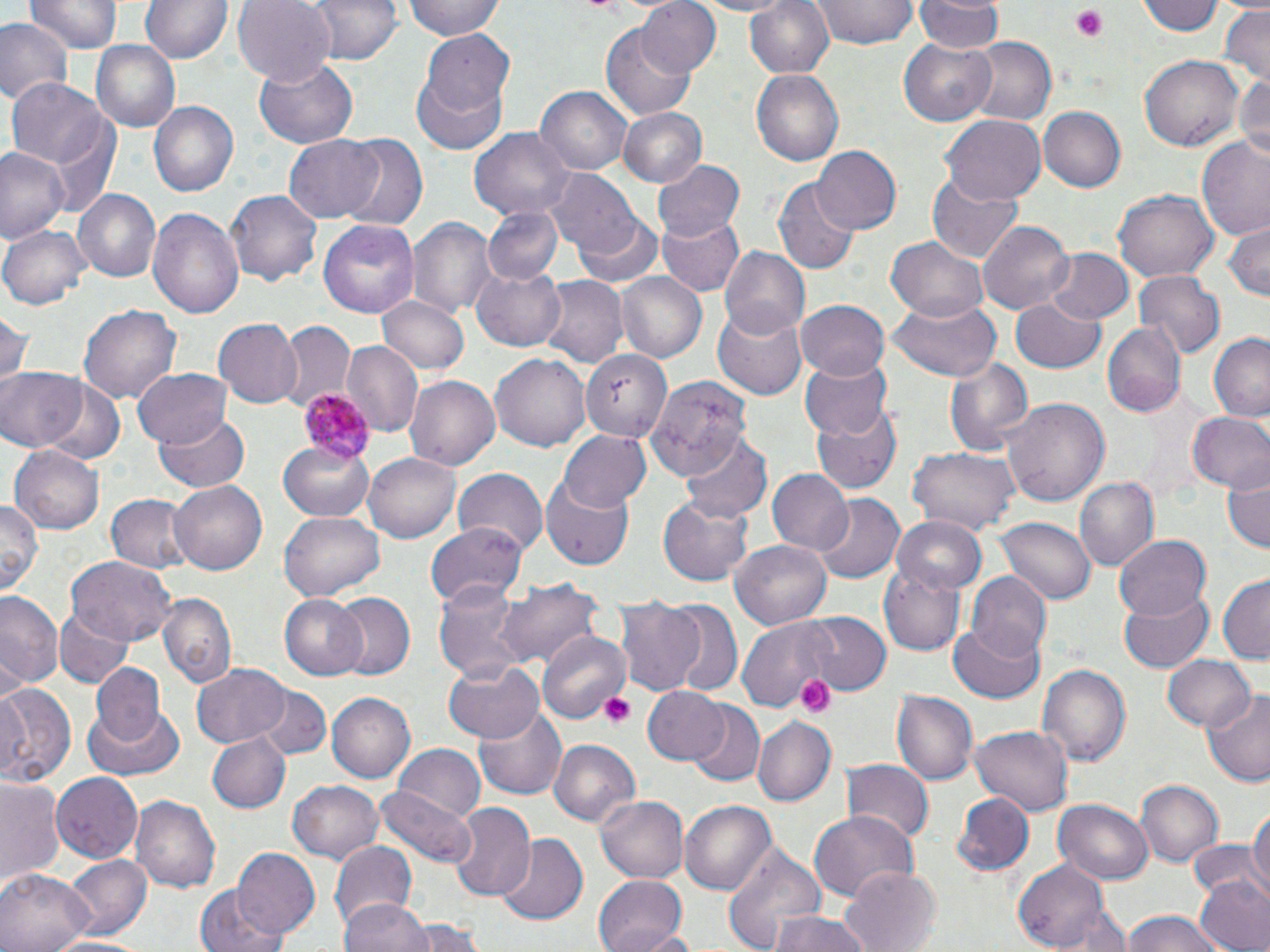 Approximate bounding boxes as (x1, y1, x2, y2) in pixels. Uninfected red blood cell locations: (27, 0, 120, 54), (139, 0, 233, 64), (232, 0, 335, 85), (305, 0, 404, 64), (402, 0, 507, 41), (636, 0, 721, 79), (684, 0, 803, 17), (742, 0, 835, 80), (812, 0, 917, 50), (1138, 0, 1225, 38), (915, 1, 1003, 55), (415, 3, 505, 82), (1217, 4, 1270, 86), (0, 18, 72, 103), (602, 22, 696, 121), (418, 29, 514, 118), (965, 38, 1056, 125), (898, 40, 994, 125), (91, 42, 179, 134), (1141, 54, 1244, 152), (254, 58, 359, 149), (414, 65, 509, 155), (750, 69, 844, 166), (7, 76, 112, 177), (1232, 77, 1269, 162), (536, 85, 634, 177), (149, 100, 240, 197), (1040, 105, 1127, 193), (616, 108, 706, 187), (942, 114, 1046, 205), (470, 129, 574, 221), (283, 132, 386, 223), (336, 133, 430, 228), (1196, 137, 1270, 243), (813, 145, 902, 234), (0, 146, 67, 244), (653, 160, 748, 243), (925, 170, 1025, 265), (549, 172, 643, 259), (775, 177, 860, 274), (73, 189, 162, 284), (225, 190, 324, 285), (1112, 191, 1219, 284), (149, 205, 245, 323), (483, 208, 562, 285), (573, 209, 665, 290), (657, 216, 747, 296), (409, 217, 495, 317), (1224, 218, 1269, 301), (319, 220, 420, 318), (979, 220, 1073, 316), (1, 225, 91, 309), (888, 236, 990, 321), (720, 247, 811, 340), (1043, 248, 1132, 328), (474, 264, 568, 351), (613, 269, 707, 362), (1134, 271, 1225, 360), (538, 274, 628, 369), (377, 295, 469, 376), (886, 296, 1002, 383), (796, 298, 893, 381), (1011, 299, 1107, 375), (80, 304, 182, 405), (713, 304, 810, 397), (0, 308, 30, 390), (215, 318, 304, 408), (276, 320, 355, 409), (1103, 320, 1185, 419), (1208, 332, 1270, 421), (577, 338, 669, 443), (344, 341, 422, 438), (491, 353, 590, 452), (801, 355, 893, 437), (945, 356, 1032, 457), (133, 366, 230, 449), (0, 367, 84, 452), (405, 374, 500, 472), (647, 379, 749, 480), (40, 381, 125, 467), (1003, 396, 1109, 509), (812, 403, 903, 494), (153, 411, 247, 492), (1185, 412, 1270, 494), (556, 428, 652, 512), (681, 433, 771, 522), (277, 441, 376, 521), (10, 444, 105, 533), (909, 448, 1019, 533), (365, 450, 465, 544), (455, 469, 546, 552), (769, 469, 854, 553), (1222, 469, 1268, 554), (1074, 476, 1159, 570), (540, 477, 634, 569), (169, 479, 269, 574), (812, 492, 904, 585), (105, 493, 191, 570), (658, 497, 754, 586), (0, 499, 41, 593), (281, 513, 384, 600), (997, 514, 1097, 604), (893, 518, 987, 596), (425, 521, 527, 608), (1116, 535, 1213, 620), (731, 539, 832, 629), (66, 556, 176, 649), (880, 565, 966, 657), (967, 572, 1052, 661), (1217, 574, 1270, 663), (500, 577, 604, 674), (434, 580, 527, 681), (1119, 588, 1214, 673), (0, 593, 62, 692), (156, 593, 236, 686), (330, 594, 415, 681), (278, 595, 370, 680), (613, 597, 707, 698), (661, 599, 743, 695), (53, 606, 134, 689), (737, 612, 872, 708), (805, 614, 892, 696), (949, 622, 1045, 704), (537, 631, 629, 724), (1162, 655, 1257, 734), (443, 661, 547, 743), (92, 662, 166, 746), (192, 663, 291, 746), (1037, 663, 1132, 766), (0, 682, 74, 787), (257, 683, 330, 758), (643, 686, 731, 765), (1203, 689, 1270, 787), (893, 690, 977, 785), (327, 692, 416, 784), (82, 700, 185, 783), (475, 700, 567, 799), (684, 702, 764, 786), (754, 718, 836, 806), (973, 726, 1072, 816), (206, 732, 291, 813), (549, 739, 640, 828), (392, 746, 484, 826), (842, 760, 932, 845), (51, 773, 143, 865), (0, 776, 66, 896), (287, 780, 386, 863), (1135, 780, 1224, 866), (375, 786, 476, 869), (950, 792, 1035, 879), (594, 795, 688, 885), (132, 796, 220, 892), (1054, 798, 1153, 884), (680, 799, 776, 896), (449, 802, 536, 902), (1249, 803, 1269, 905), (808, 810, 917, 900), (496, 832, 586, 925), (328, 840, 418, 933), (720, 841, 827, 952), (231, 849, 322, 942), (62, 856, 150, 941), (1010, 863, 1123, 951), (842, 868, 942, 951), (0, 869, 95, 952), (593, 874, 689, 952), (1193, 875, 1270, 952), (195, 884, 288, 952), (341, 898, 435, 952), (1118, 909, 1235, 952), (766, 910, 876, 952), (403, 917, 484, 950), (48, 935, 158, 952). Platelet locations: (1072, 6, 1109, 41), (795, 674, 837, 717), (601, 692, 636, 729). Plasmodium malariae-infected red blood cell locations: (298, 390, 377, 462). Slide-level diagnosis: Plasmodium malariae. Optical microscopy. Thin blood film. 1000x magnification. One field of a larger specimen. May-Grünwald-Giemsa stain. Image is 1270×952 pixels.